Report the malaria status of this cell.
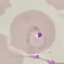
Parasitized.

image_type: automatically extracted cell patch, resized to 64 × 64 pixels
stain: Giemsa
capture: smartphone through the microscope eyepiece
preparation: thin blood film